Report the malaria status of this cell.
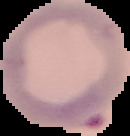
Parasitized.

image type = cell region segmented out of the field of view; surrounding area masked to black
preparation = thin blood film
image size = 130×136 pixels